Classify this cell by malaria status.
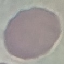

It is uninfected.

Summary:
  - Capture: smartphone camera at the microscope eyepiece
  - Preparation: thin blood film
  - Stain: Giemsa
  - Image type: cell patch, automatically extracted from a larger field of view and resized to 64 × 64 pixels